State which parasite is depicted.
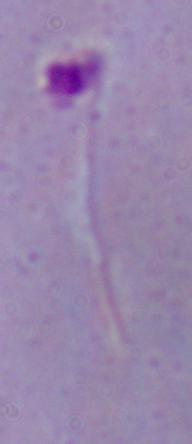
Leishmania.

Micrograph. Captured at 1000x magnification.